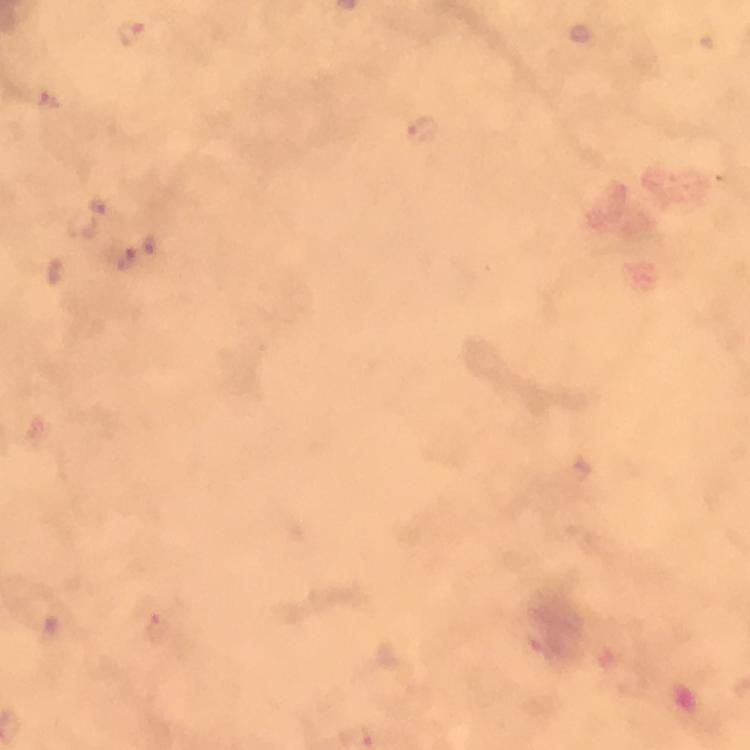

Approximate centers as {x, y} in pixels. Malaria parasite locations: {130, 34}. Thick blood smear. Giemsa-stained preparation. Image is 750×750 pixels. From a malaria diagnostic workup. A crop from one field of view. Photographed with a smartphone mounted on the microscope. 100x magnification. Immersion oil was used.